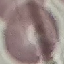

Summary:
  - Malaria status: uninfected
  - Stain: Giemsa
  - Capture: smartphone camera at the microscope eyepiece
  - Image type: cell patch, automatically extracted from a larger field of view and resized to 64 × 64 pixels
  - Preparation: thin blood film